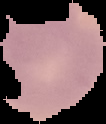
result = no malaria parasites detected
preparation = thin blood film
image type = segmented cell region on a black background
image size = 106×124 pixels